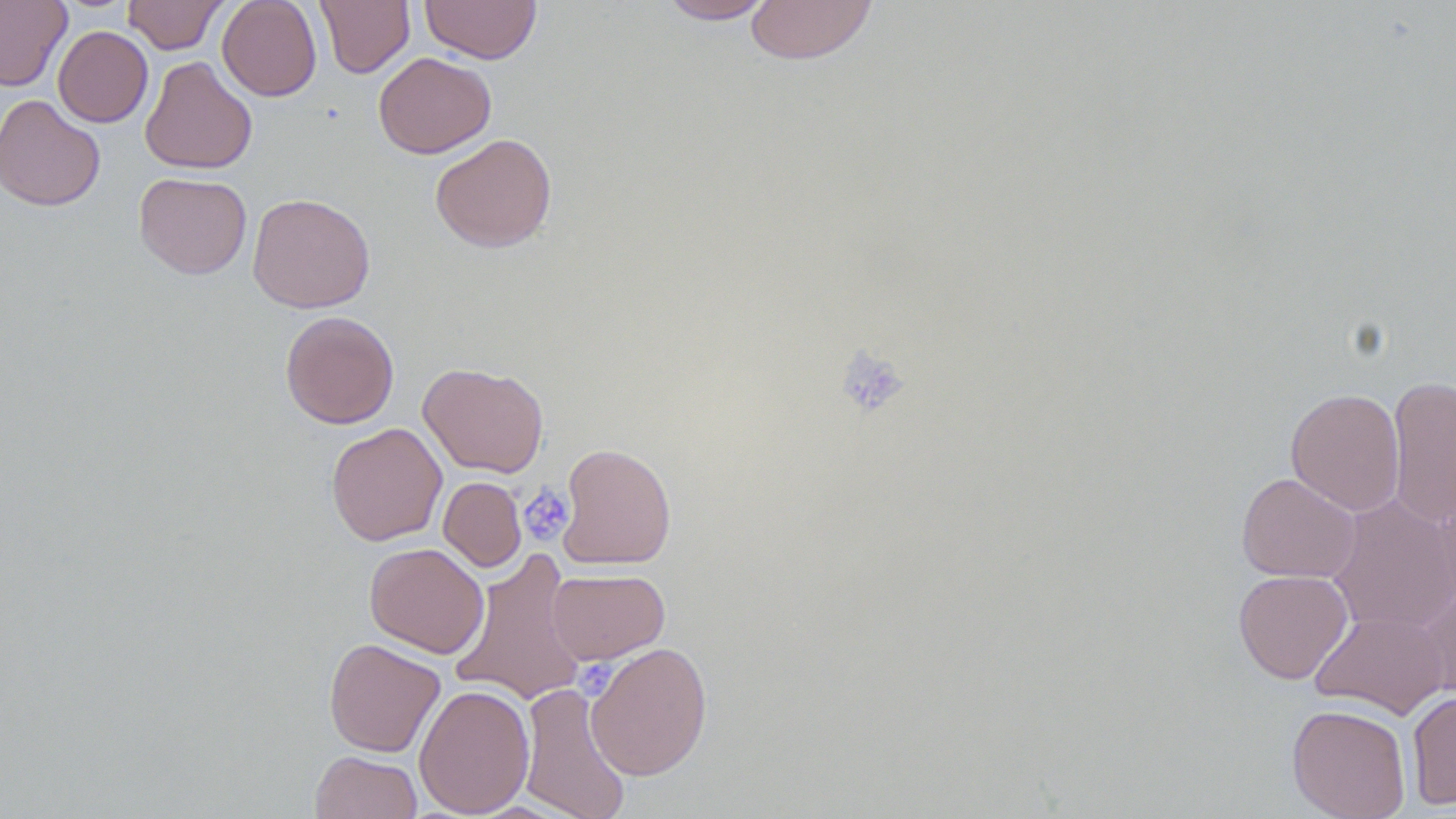

slide_level_diagnosis: no evidence of blood parasites
platelet_locations: 'approximate bounding boxes as named x1/y1/x2/y2 corners in pixels: (x1=834, y1=346, x2=910, y2=419), (x1=518, y1=485, x2=575, y2=545), (x1=576, y1=659, x2=630, y2=705)'
preparation: thin blood smear
field_of_view: one of a larger specimen
image_size: 1456×819 pixels
magnification: 1000x
stain: May-Grünwald-Giemsa
uninfected_red_blood_cell_locations: 'approximate bounding boxes as named x1/y1/x2/y2 corners in pixels: (x1=0, y1=0, x2=71, y2=92), (x1=122, y1=0, x2=228, y2=54), (x1=217, y1=0, x2=322, y2=101), (x1=315, y1=0, x2=415, y2=78), (x1=420, y1=0, x2=541, y2=64), (x1=656, y1=0, x2=777, y2=24), (x1=744, y1=0, x2=879, y2=65), (x1=53, y1=25, x2=153, y2=128), (x1=374, y1=52, x2=496, y2=158), (x1=139, y1=56, x2=257, y2=175), (x1=0, y1=94, x2=105, y2=211), (x1=430, y1=133, x2=558, y2=252), (x1=134, y1=172, x2=252, y2=279), (x1=247, y1=193, x2=375, y2=313), (x1=280, y1=311, x2=399, y2=429), (x1=418, y1=362, x2=549, y2=478), (x1=1387, y1=374, x2=1456, y2=530), (x1=1285, y1=387, x2=1405, y2=516), (x1=326, y1=422, x2=447, y2=546), (x1=556, y1=442, x2=676, y2=569), (x1=1235, y1=472, x2=1361, y2=583), (x1=438, y1=477, x2=526, y2=571), (x1=1326, y1=494, x2=1456, y2=634), (x1=364, y1=542, x2=488, y2=658), (x1=450, y1=550, x2=587, y2=707), (x1=546, y1=568, x2=670, y2=664), (x1=1233, y1=569, x2=1353, y2=684), (x1=1414, y1=584, x2=1456, y2=699), (x1=1310, y1=609, x2=1449, y2=719), (x1=323, y1=638, x2=446, y2=757), (x1=585, y1=641, x2=713, y2=780), (x1=517, y1=681, x2=632, y2=819), (x1=414, y1=684, x2=535, y2=817), (x1=1406, y1=690, x2=1456, y2=810), (x1=1286, y1=704, x2=1411, y2=819), (x1=310, y1=750, x2=422, y2=819)'
modality: optical microscopy